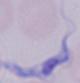 A trypanosome is seen. 1000x magnification. Photomicrograph.